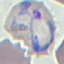
{
  "malaria_status": "parasitized",
  "image_type": "automatically extracted cell patch, resized to 64 × 64 pixels",
  "stain": "Giemsa",
  "preparation": "thin blood smear",
  "capture": "smartphone camera at the microscope eyepiece"
}